Assess this cell for malaria.
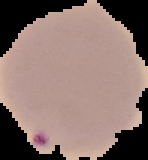

It is parasitized.

preparation = thin blood smear
image size = 148×160 pixels
image type = cell region segmented out of the field of view; surrounding area masked to black